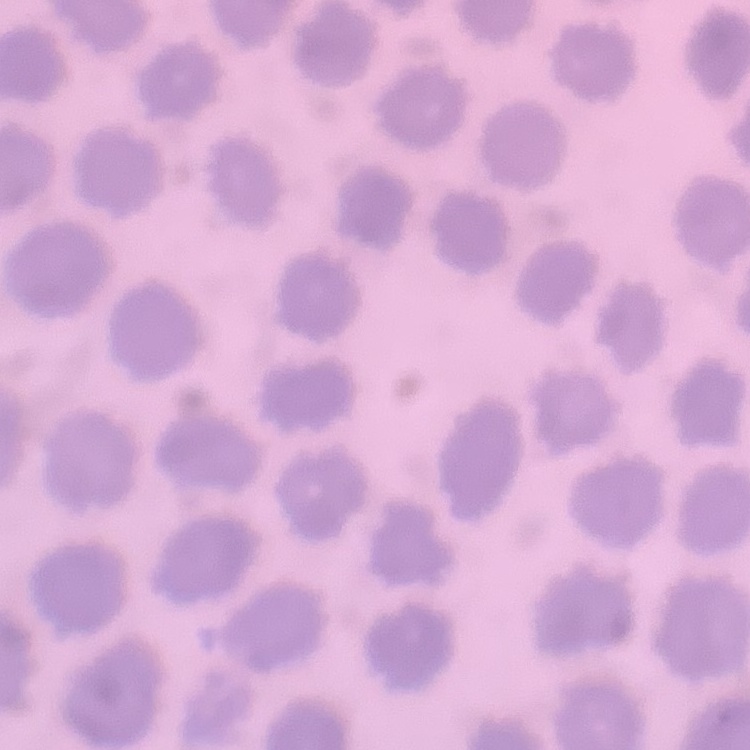

Summary:
  - Erythrocyte morphology: no rouleaux formation
  - Stain: Field's or Giemsa
  - Image type: square crop of a larger photomicrograph
  - Preparation: thin peripheral smear